Report the malaria status of this cell.
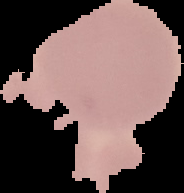
Uninfected.

image type = segmented cell region with the area outside set to black
image size = 184×193 pixels
preparation = thin blood smear